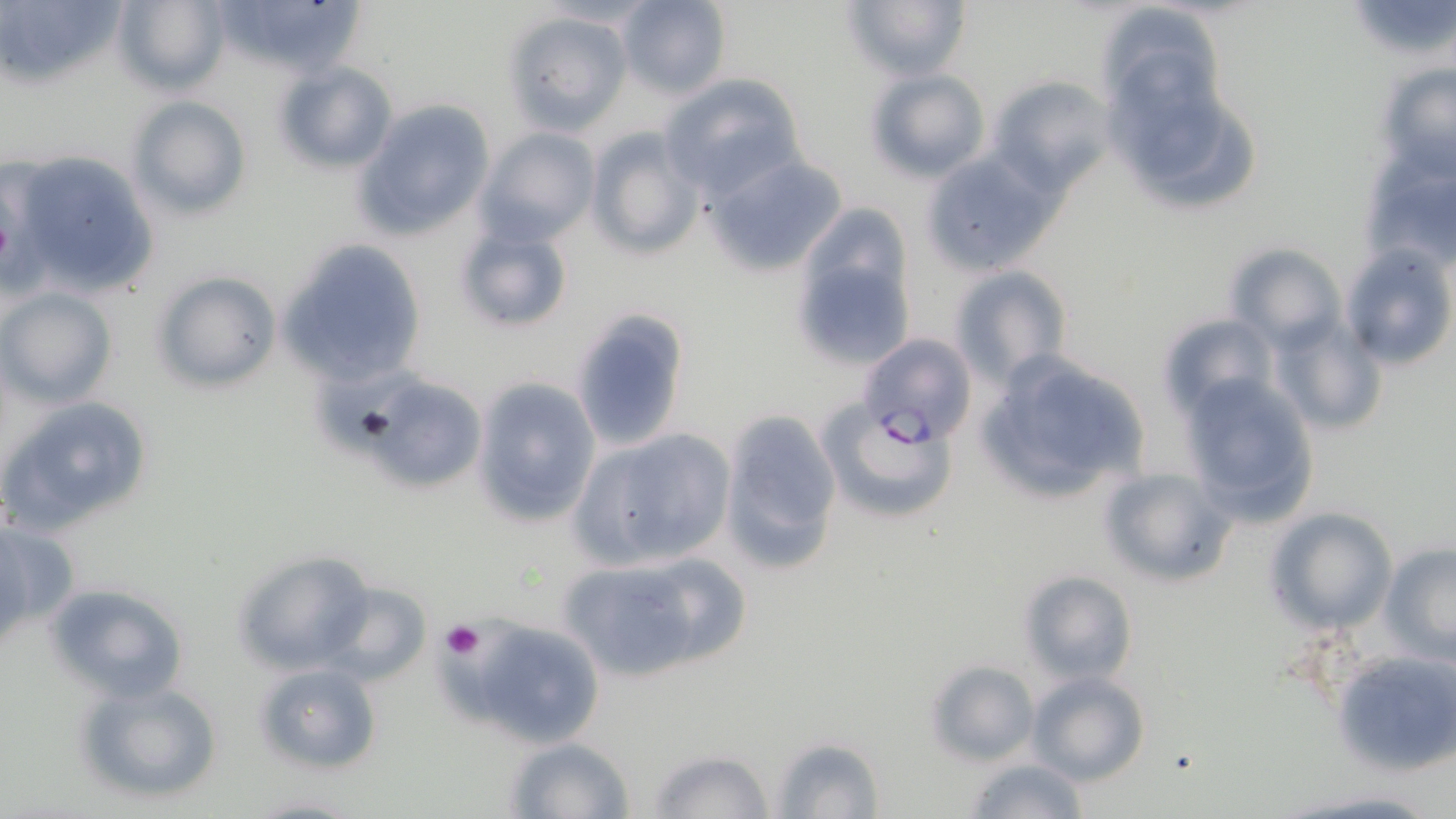

Approximate bounding boxes as (x1, y1, x2, y2) in pixels. Platelet locations: (442, 621, 485, 661). Plasmodium falciparum-infected red blood cell locations: (859, 332, 976, 446). Uninfected red blood cell locations: (113, 0, 229, 97), (206, 0, 371, 79), (613, 0, 732, 97), (841, 0, 972, 81), (1094, 0, 1227, 119), (1346, 0, 1456, 65), (8, 2, 133, 83), (503, 9, 633, 135), (273, 61, 398, 175), (1375, 63, 1456, 182), (1103, 65, 1266, 219), (865, 69, 991, 183), (659, 72, 806, 200), (985, 74, 1117, 194), (127, 96, 251, 221), (354, 99, 493, 239), (476, 127, 601, 245), (585, 127, 705, 261), (917, 149, 1061, 276), (4, 152, 160, 301), (702, 154, 850, 278), (1366, 156, 1454, 272), (451, 217, 574, 336), (793, 222, 916, 369), (280, 239, 426, 384), (1342, 243, 1455, 371), (1227, 245, 1346, 349), (948, 265, 1073, 387), (152, 272, 281, 393), (1, 286, 117, 407), (567, 305, 698, 487), (1161, 313, 1277, 417), (1275, 317, 1388, 438), (970, 347, 1153, 509), (1177, 372, 1320, 524), (349, 375, 489, 493), (471, 377, 603, 529), (1, 396, 157, 533), (818, 400, 960, 527), (719, 409, 842, 575), (570, 425, 737, 569), (1098, 466, 1235, 586), (1266, 507, 1395, 634), (0, 520, 80, 635), (1380, 542, 1456, 661), (232, 549, 376, 675), (555, 549, 747, 683), (1018, 570, 1138, 685), (319, 581, 432, 687), (46, 582, 187, 702), (463, 619, 602, 748), (1332, 645, 1456, 780), (923, 659, 1041, 767), (252, 661, 382, 777), (1026, 671, 1150, 787), (72, 676, 224, 806), (768, 735, 883, 817), (502, 737, 637, 819), (645, 748, 777, 819), (962, 758, 1094, 818), (1279, 786, 1448, 818), (244, 792, 362, 818). Slide-level diagnosis: Plasmodium falciparum. Thin blood smear. Image is 1456×819 pixels. One field of a larger specimen. Optical microscopy. Captured at 1000x magnification. May-Grünwald-Giemsa-stained preparation.